Name the blood parasite species.
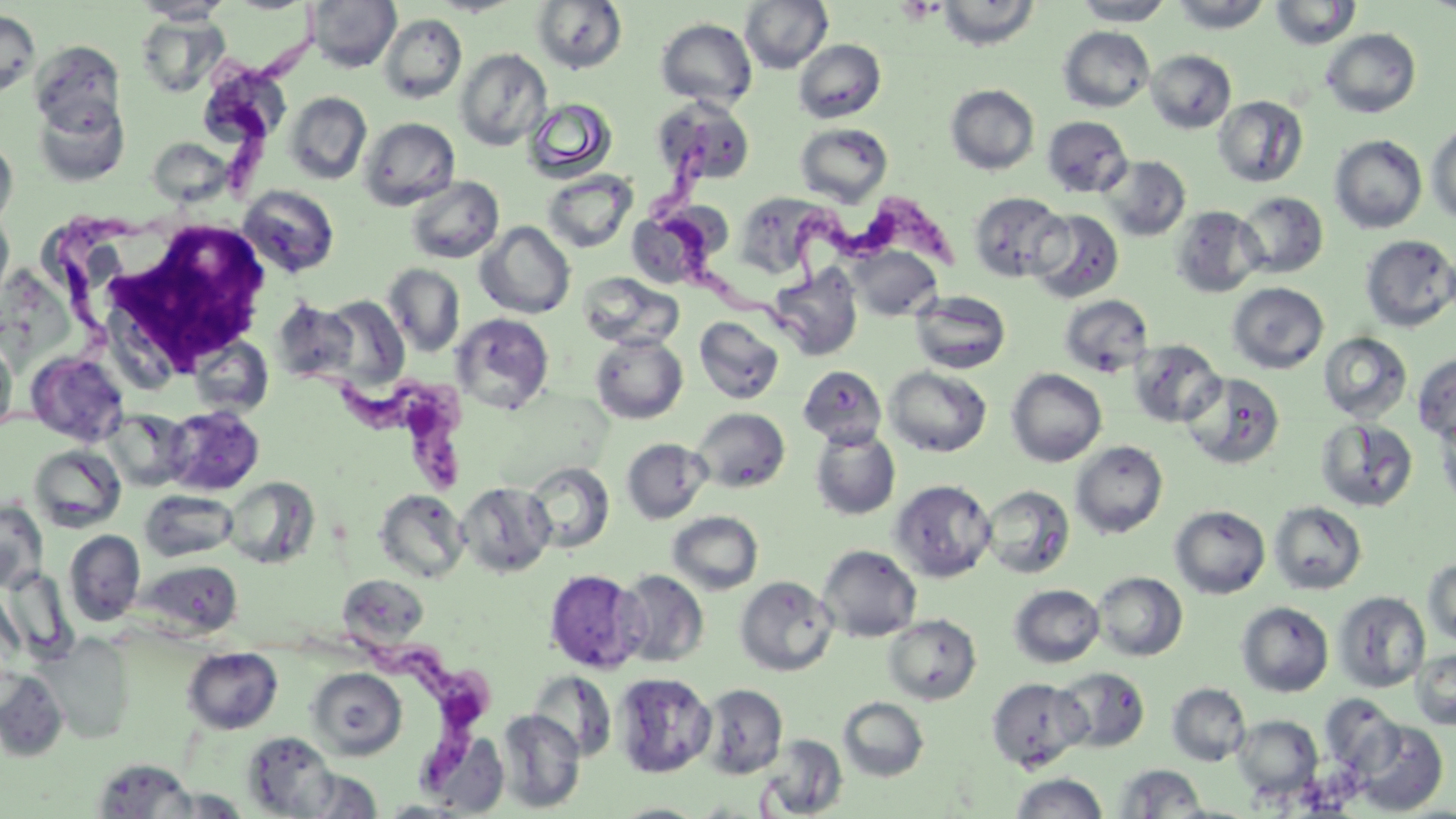
Trypanosoma brucei.

Approximate bounding boxes as (x1,y1)-(x2,y2) corner pairs in pixels. White blood cell locations: (107,217)-(274,372). Uninfected red blood cell locations: (133,0)-(234,23), (307,0)-(400,73), (431,0)-(523,17), (740,0)-(833,74), (936,0)-(1040,50), (1073,0)-(1175,26), (1170,0)-(1273,33), (1270,0)-(1361,50), (531,1)-(627,74), (0,10)-(40,97), (378,13)-(467,105), (136,14)-(230,98), (656,18)-(757,109), (1058,26)-(1154,112), (1321,29)-(1421,118), (793,39)-(886,123), (30,41)-(125,133), (454,48)-(552,151), (1146,50)-(1236,133), (197,61)-(291,147), (945,84)-(1040,175), (285,92)-(372,185), (34,96)-(130,186), (1214,96)-(1308,187), (523,97)-(618,183), (654,98)-(755,187), (1042,115)-(1133,198), (359,117)-(460,210), (795,122)-(893,207), (1426,122)-(1456,225), (0,135)-(18,232), (1330,135)-(1427,233), (148,137)-(232,205), (1099,155)-(1191,241), (542,170)-(638,253), (406,176)-(504,264), (239,185)-(339,277), (747,185)-(820,275), (969,192)-(1069,282), (1236,192)-(1328,278), (1170,206)-(1266,297), (0,209)-(14,308), (1028,209)-(1124,304), (627,210)-(712,289), (476,221)-(575,319), (1360,234)-(1456,332), (851,246)-(941,321), (383,263)-(465,357), (768,265)-(863,361), (578,272)-(684,351), (1228,282)-(1329,374), (911,290)-(1011,374), (1059,294)-(1154,376), (317,295)-(410,392), (273,298)-(360,387), (451,313)-(554,415), (694,316)-(784,405), (1318,332)-(1412,424), (590,334)-(688,424), (0,336)-(17,434), (189,337)-(273,417), (1129,340)-(1225,427), (26,351)-(129,446), (1413,353)-(1456,447), (798,365)-(887,447), (885,367)-(992,457), (1007,369)-(1107,467), (1182,372)-(1286,469), (162,405)-(265,496), (691,407)-(790,493), (103,409)-(191,491), (1436,409)-(1456,514), (1316,418)-(1418,513), (810,427)-(901,520), (621,438)-(711,523), (1071,441)-(1168,538), (30,444)-(125,532), (524,462)-(615,553), (223,477)-(318,570), (890,479)-(997,582), (457,481)-(556,578), (981,484)-(1075,579), (140,489)-(239,562), (374,489)-(469,583), (0,499)-(49,594), (1269,501)-(1367,594), (1170,505)-(1270,599), (668,511)-(764,594), (64,529)-(146,626), (818,544)-(922,642), (1423,558)-(1456,648), (140,559)-(242,639), (544,568)-(646,672), (614,569)-(709,668), (1093,572)-(1187,661), (338,574)-(430,648), (735,575)-(838,676), (1009,584)-(1105,668), (1333,591)-(1430,693), (1237,602)-(1333,697), (884,614)-(981,704), (44,635)-(135,743), (183,647)-(282,734), (1411,648)-(1456,730), (307,667)-(407,759), (1055,667)-(1150,752), (0,669)-(69,761), (528,669)-(619,761), (614,672)-(717,778), (986,676)-(1092,772), (698,683)-(788,778), (1168,683)-(1251,766), (838,697)-(929,781), (496,709)-(585,813), (1232,715)-(1322,800), (1348,719)-(1450,815), (419,729)-(510,816), (241,732)-(340,817), (757,734)-(848,818), (91,758)-(200,818), (1114,764)-(1210,817), (294,770)-(385,817), (1009,772)-(1109,818), (159,788)-(252,818), (610,802)-(708,818). Trypanosoma brucei locations: (216,38)-(330,202), (649,131)-(811,353), (779,188)-(964,305), (4,203)-(164,432), (287,362)-(477,498), (306,631)-(504,802). Platelet locations: (897,0)-(942,23). Image is 1456×819 pixels. Single field of view. Optical microscopy. Thin blood smear. Captured at 1000x magnification. May-Grünwald-Giemsa-stained preparation.